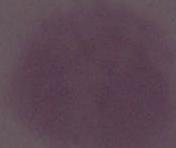
modality: photomicrograph
magnification: 1000x
identification: red blood cell